Give the extent of all Plasmodium vivax-infected red blood cells.
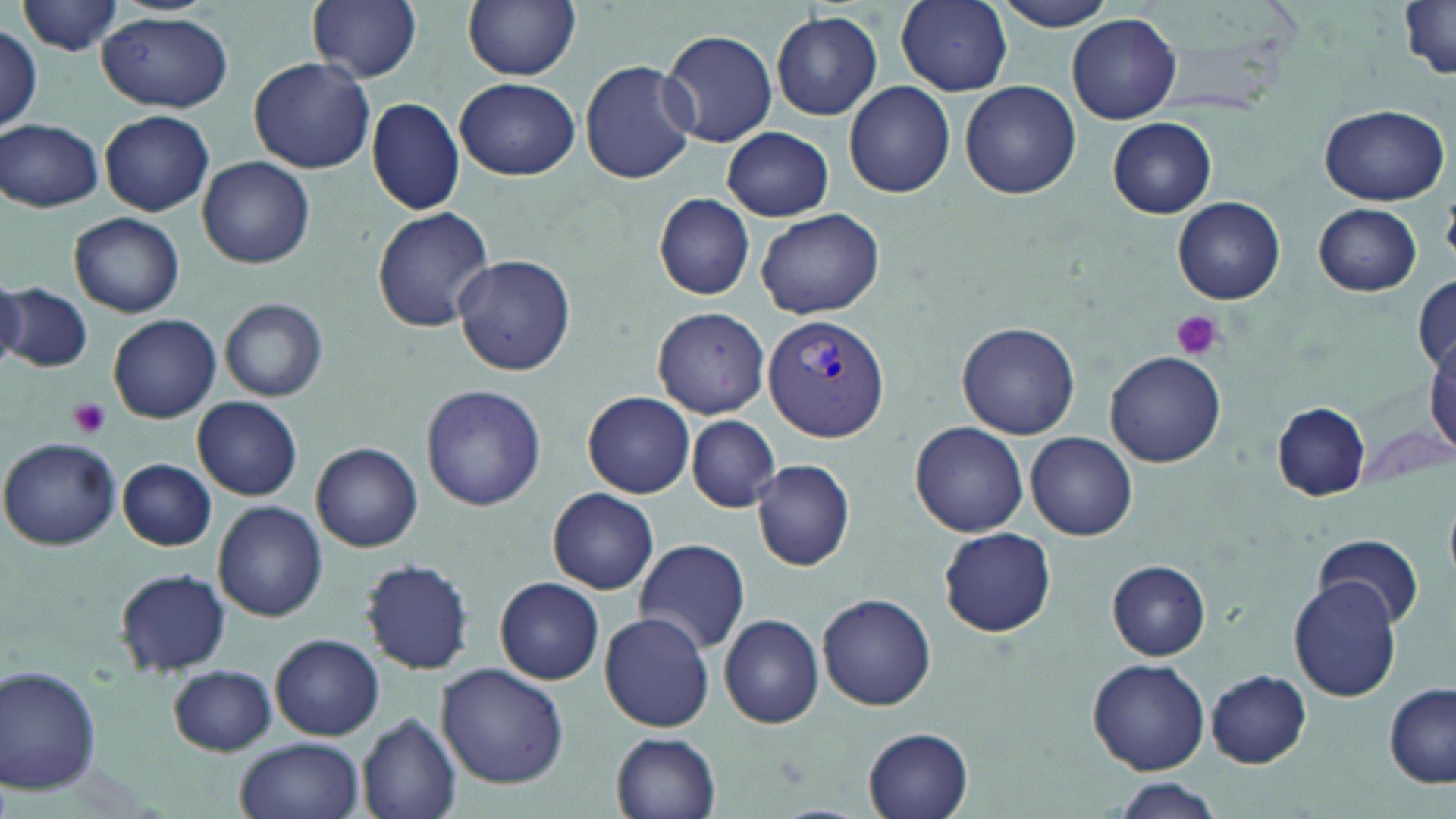

Approximate bounding boxes as (x1,y1)-(x2,y2) corner pairs in pixels.
Plasmodium vivax-infected red blood cells: (764,317)-(892,442).

Uninfected red blood cell locations: (309,0)-(422,83), (463,0)-(581,80), (896,0)-(1012,94), (990,0)-(1125,31), (22,1)-(122,57), (1398,5)-(1456,80), (771,11)-(882,120), (99,14)-(234,112), (1067,14)-(1181,124), (1,24)-(42,130), (661,28)-(777,148), (247,57)-(375,173), (579,59)-(698,184), (455,77)-(579,180), (844,81)-(955,198), (960,81)-(1081,200), (367,98)-(464,215), (1320,103)-(1452,204), (100,110)-(214,216), (1107,116)-(1217,218), (2,118)-(105,210), (722,127)-(834,221), (198,156)-(315,269), (654,193)-(755,301), (1173,197)-(1284,305), (1314,203)-(1421,296), (372,206)-(495,333), (756,209)-(884,319), (70,213)-(184,318), (81,222)-(197,395), (453,253)-(578,376), (0,273)-(26,371), (1413,275)-(1456,375), (3,281)-(93,374), (221,298)-(327,402), (651,306)-(772,420), (108,314)-(221,423), (957,321)-(1081,440), (1105,352)-(1225,467), (420,384)-(546,510), (583,392)-(695,498), (193,397)-(302,500), (1271,402)-(1369,500), (686,416)-(778,511), (1356,418)-(1454,495), (910,422)-(1029,535), (1026,432)-(1137,541), (1,436)-(122,550), (313,442)-(424,550), (119,459)-(216,552), (751,459)-(856,571), (548,488)-(659,595), (213,501)-(329,620), (938,527)-(1056,637), (1315,534)-(1423,629), (633,539)-(749,655), (360,558)-(475,676), (1107,561)-(1210,660), (114,568)-(231,676), (493,578)-(608,687), (1289,579)-(1400,701), (817,593)-(938,711), (600,610)-(717,732), (719,614)-(825,728), (272,635)-(383,741), (1088,657)-(1209,774), (437,663)-(568,788), (0,665)-(102,795), (168,665)-(277,756), (1207,671)-(1311,767), (1384,685)-(1455,787), (356,713)-(461,819), (861,726)-(976,819), (610,732)-(720,819), (235,737)-(363,819), (1106,777)-(1226,818). Platelet locations: (1169,309)-(1225,362), (69,398)-(110,437). Slide-level diagnosis: Plasmodium vivax. Optical microscopy. Single field of view. May-Grünwald-Giemsa-stained preparation. Captured at 1000x magnification. Thin blood film. Image is 1456×819 pixels.